State the preparation type.
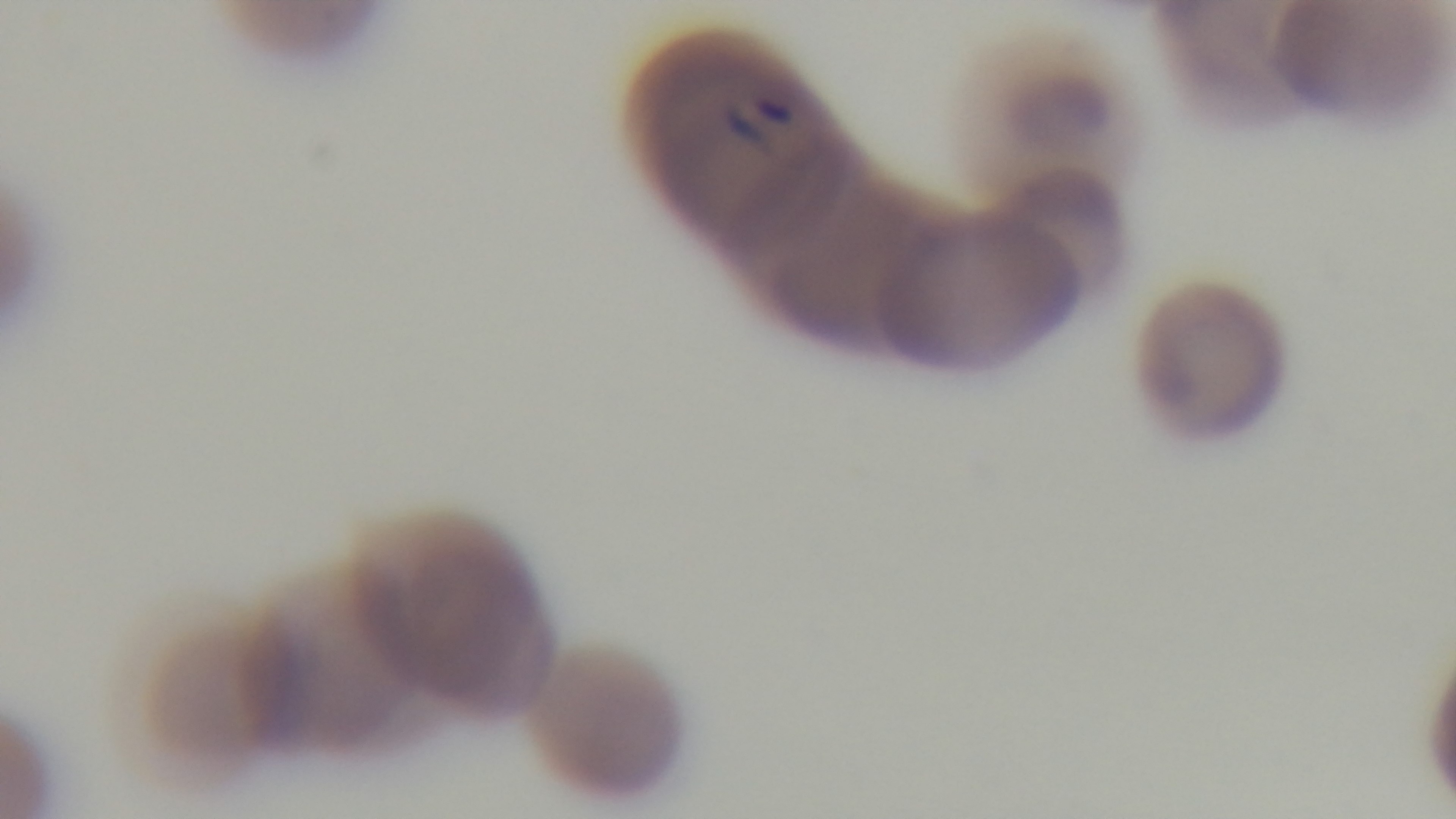

A thin smear.

Mounted 4K digital camera. Giemsa-stained. Malaria status: infected. Single field of view. Photomicrograph. Oil-immersion objective, 100x.